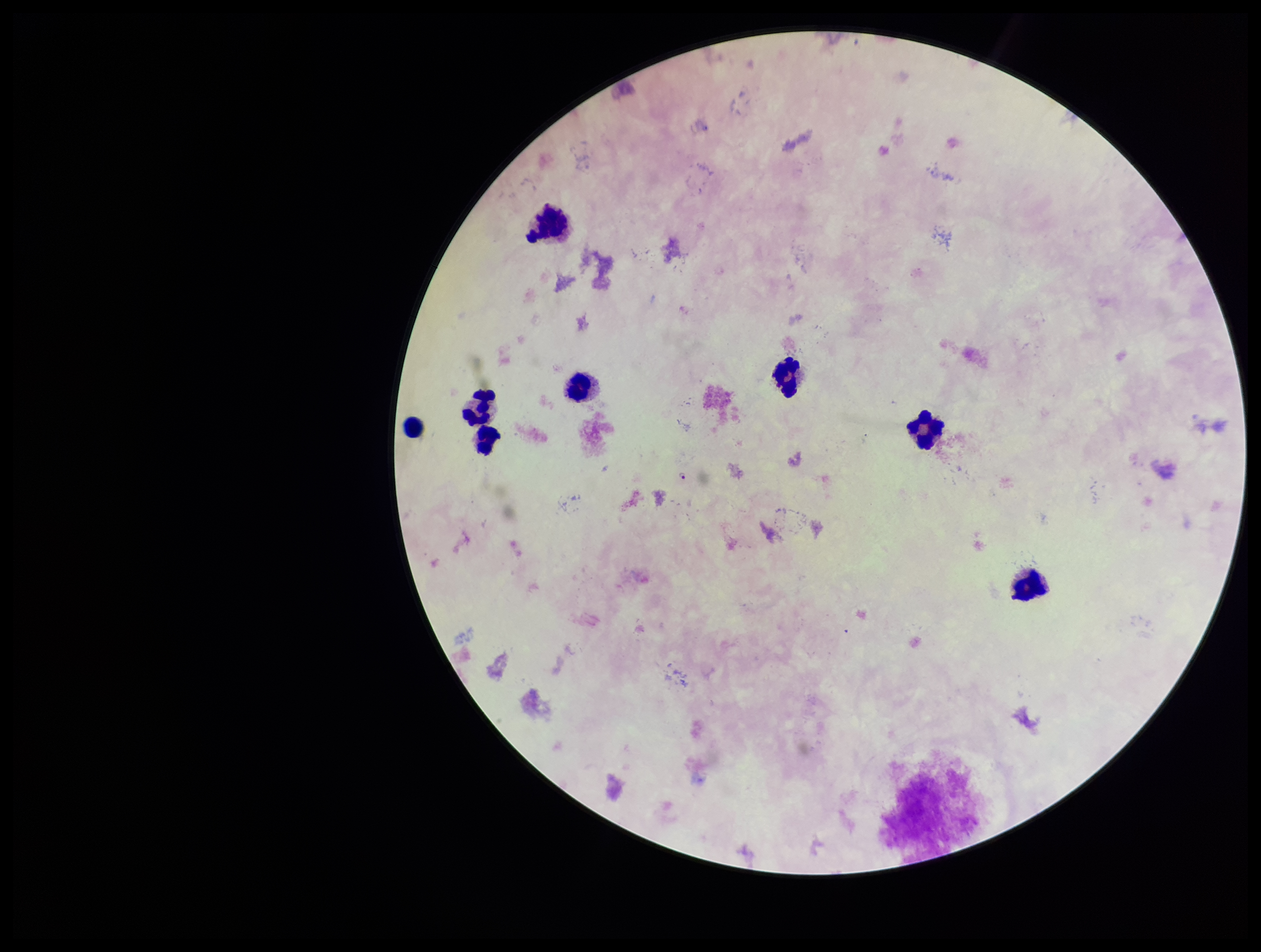
capture = smartphone photograph through the microscope eyepiece
image size = 1261×952 pixels
stain = Giemsa
leukocyte count = 8
parasite count = 1
preparation = thick smear
field of view = single
species reported for this patient = Plasmodium falciparum
Plasmodium parasites = detected
patient malaria status = infected